Assess this cell for malaria.
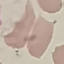
It is uninfected.

stain = Giemsa
preparation = thin blood film
image type = cell patch, automatically extracted from a larger field of view and resized to 64 × 64 pixels
capture = smartphone through the microscope eyepiece